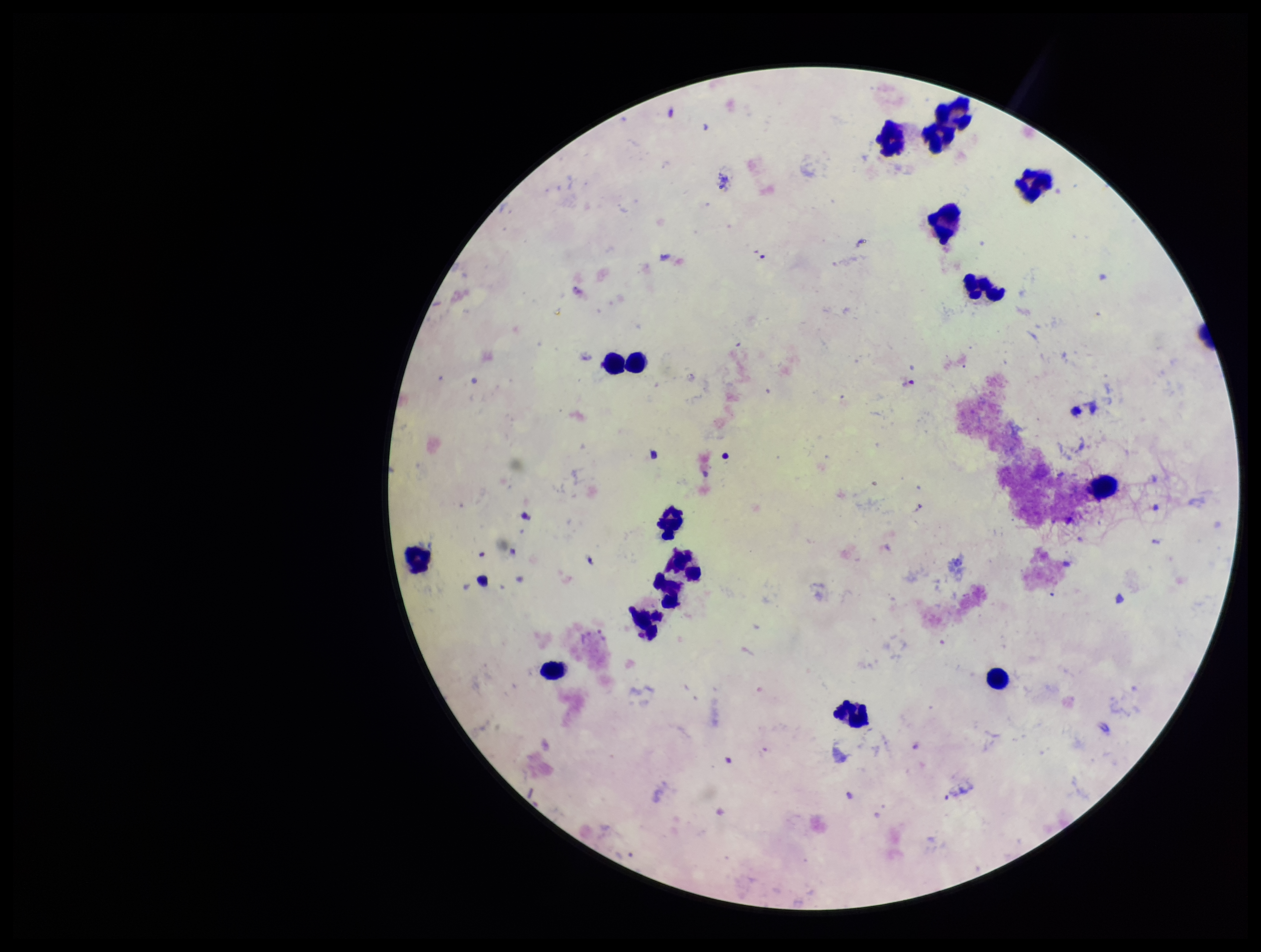

Summary:
  - Stain: Giemsa
  - Preparation: thick
  - Leukocyte count: 17
  - Patient malaria status: negative
  - Field of view: one from this slide
  - Capture: smartphone photograph through the microscope eyepiece
  - Parasite count: 0
  - Image size: 1261×952 pixels
  - Plasmodium parasites: none seen